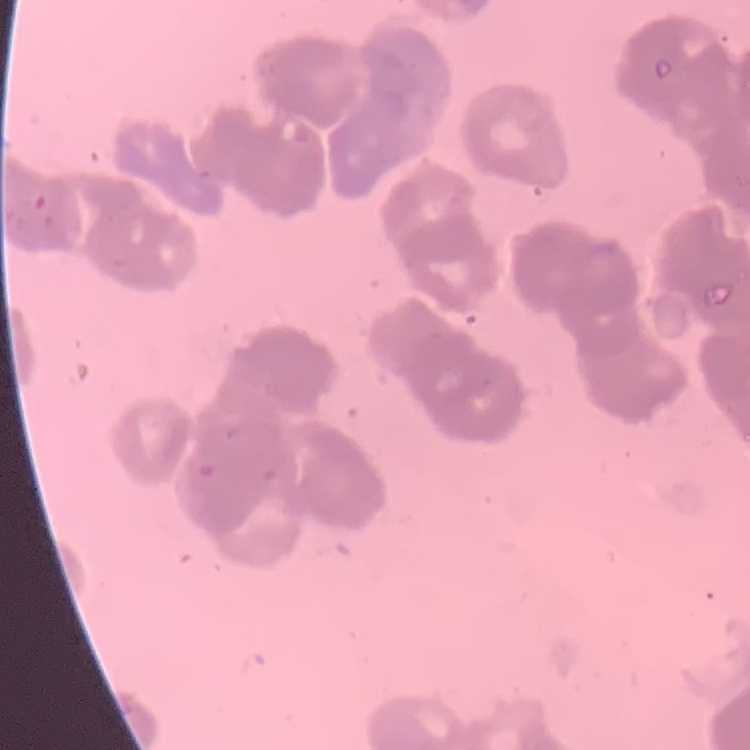
{
  "red_blood_cell_morphology": "rouleaux formation",
  "stain": "Field's or Giemsa",
  "preparation": "thin blood smear",
  "image_type": "one tile cut from a larger photomicrograph"
}